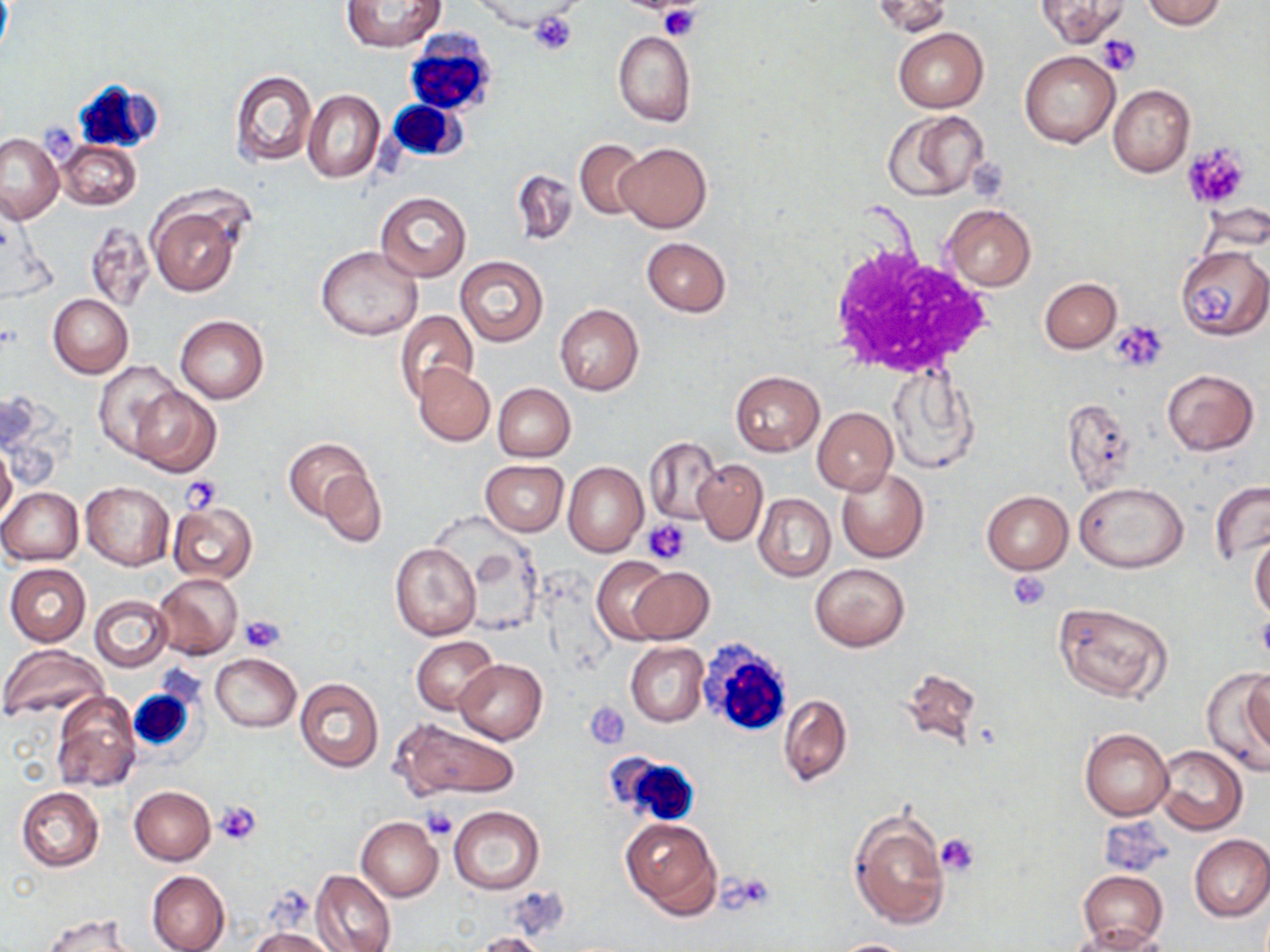

{
  "slide_level_diagnosis": "negative for blood parasites",
  "uninfected_red_blood_cell_locations": "approximate bounding boxes as (x1, y1, x2, y2) in pixels: (872, 0, 950, 37), (1036, 0, 1128, 47), (341, 1, 445, 52), (477, 1, 584, 37), (1142, 1, 1228, 29), (894, 28, 987, 113), (613, 30, 696, 127), (1020, 51, 1120, 148), (228, 70, 317, 167), (1108, 85, 1195, 177), (303, 89, 385, 183), (882, 110, 991, 202), (0, 133, 65, 223), (57, 139, 141, 211), (577, 139, 645, 220), (615, 143, 711, 232), (510, 169, 577, 247), (375, 192, 470, 281), (149, 199, 243, 297), (942, 204, 1036, 291), (85, 221, 156, 313), (642, 237, 731, 316), (316, 246, 424, 341), (1176, 246, 1270, 339), (455, 256, 549, 346), (1040, 278, 1121, 353), (49, 294, 133, 378), (555, 304, 643, 396), (394, 308, 478, 404), (176, 315, 268, 404), (93, 361, 182, 462), (413, 363, 494, 446), (888, 367, 980, 472), (1162, 369, 1259, 454), (731, 371, 824, 454), (493, 383, 576, 461), (130, 385, 220, 478), (1063, 399, 1138, 494), (813, 407, 897, 495), (644, 436, 722, 525), (285, 437, 368, 520), (0, 444, 16, 527), (692, 459, 768, 546), (481, 460, 567, 536), (563, 462, 648, 557), (836, 467, 929, 562), (318, 468, 386, 546), (81, 481, 174, 569), (1209, 481, 1270, 564), (1074, 482, 1188, 573), (1, 488, 83, 565), (982, 491, 1072, 574), (754, 494, 836, 581), (167, 502, 257, 584), (1250, 532, 1270, 623), (389, 543, 480, 640), (591, 557, 676, 643), (810, 562, 910, 652), (5, 563, 91, 646), (629, 567, 714, 643), (153, 572, 243, 659), (90, 596, 171, 670), (1053, 601, 1173, 702), (412, 636, 498, 715), (625, 642, 708, 726), (0, 645, 108, 721), (211, 653, 302, 732), (455, 659, 548, 744), (1203, 663, 1270, 773), (899, 666, 985, 746), (1243, 668, 1270, 762), (294, 677, 384, 772), (52, 692, 140, 792), (779, 694, 853, 786), (394, 719, 520, 800), (1079, 727, 1172, 820), (1153, 745, 1248, 835), (130, 785, 215, 865), (15, 786, 104, 872), (449, 806, 544, 894), (848, 808, 950, 929), (620, 816, 722, 920), (356, 817, 443, 899), (1189, 835, 1270, 922), (321, 836, 433, 936), (1075, 869, 1168, 948), (312, 870, 396, 952), (146, 871, 229, 952), (43, 915, 138, 952), (1064, 924, 1169, 952), (250, 927, 336, 952), (473, 931, 554, 952), (832, 938, 918, 951)",
  "platelet_locations": "approximate bounding boxes as (x1, y1, x2, y2) in pixels: (657, 2, 701, 41), (529, 11, 579, 56), (1097, 35, 1140, 75), (1182, 142, 1250, 208), (1193, 282, 1235, 325), (1111, 320, 1167, 371), (181, 478, 222, 513), (643, 519, 691, 564), (1006, 569, 1050, 610), (240, 615, 284, 653), (585, 702, 629, 748), (216, 800, 263, 844), (424, 807, 457, 840), (937, 833, 979, 876)",
  "modality": "optical microscopy",
  "magnification": "1000x",
  "preparation": "thin blood smear",
  "image_size": "1270×952 pixels",
  "field_of_view": "single",
  "stain": "May-Grünwald-Giemsa",
  "white_blood_cell_locations": "approximate bounding boxes as (x1, y1, x2, y2) in pixels: (402, 30, 500, 119), (73, 78, 161, 152), (385, 100, 465, 160), (823, 241, 996, 383), (695, 637, 795, 741), (129, 687, 197, 754), (607, 752, 702, 827)"
}